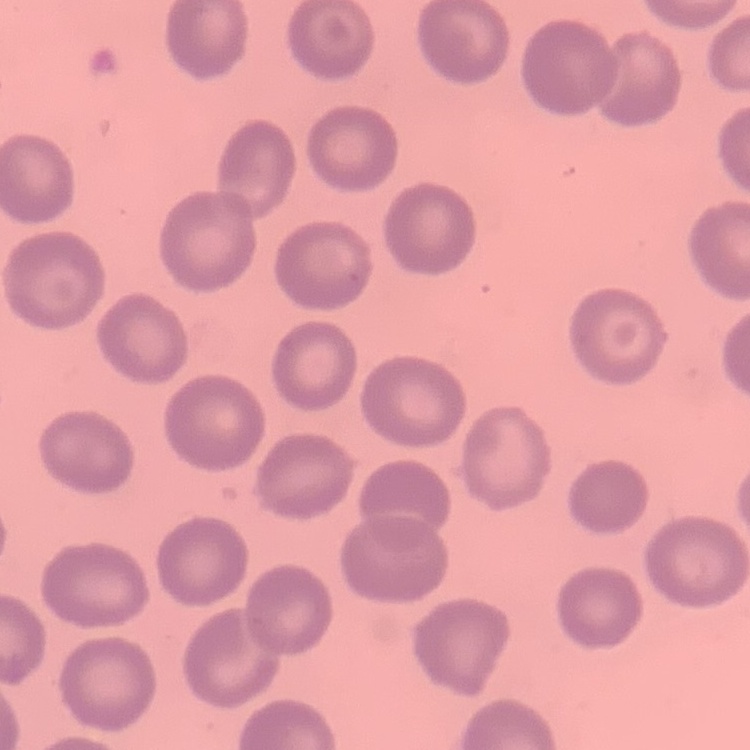
{
  "erythrocyte_morphology": "no rouleaux formation",
  "image_type": "square crop of a larger photomicrograph",
  "preparation": "thin peripheral smear",
  "stain": "Field's or Giemsa"
}